Describe the morphology of the red blood cells.
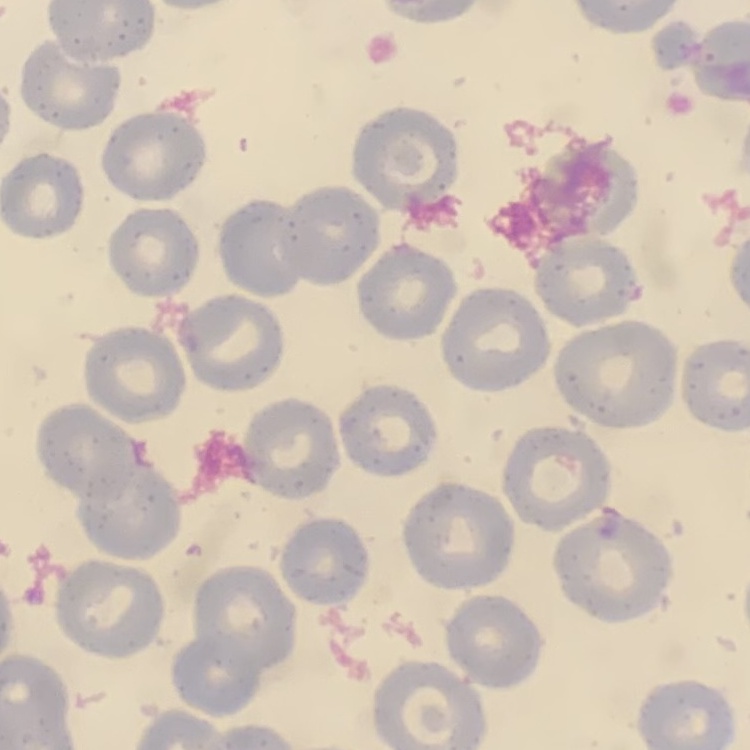
They show no rouleaux formation.

{
  "image_type": "one tile cut from a larger photomicrograph",
  "stain": "Field's or Giemsa",
  "preparation": "thin blood film"
}